Assess the morphology of the red blood cells.
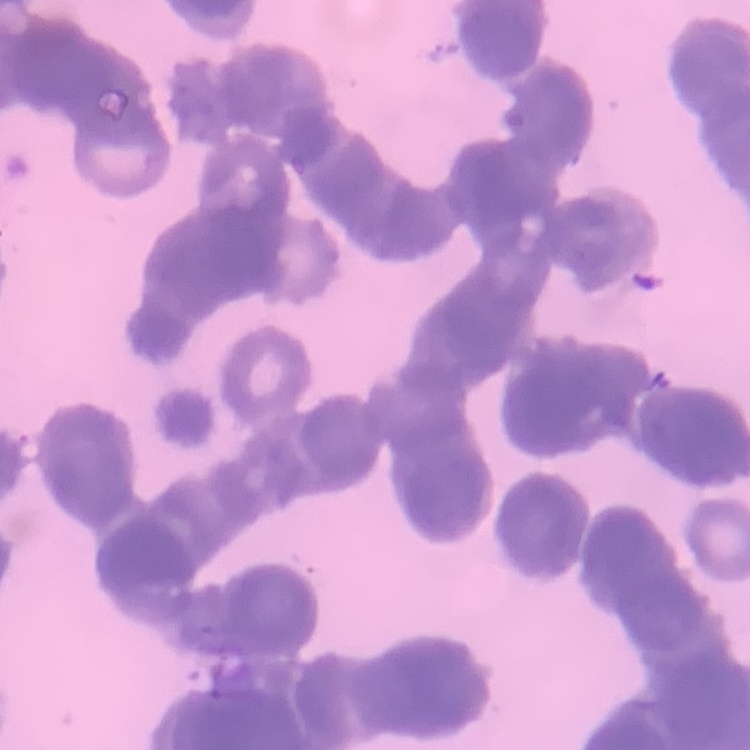
They show rouleaux formation.

Square crop of a larger photomicrograph. Stained with either Field's or Giemsa. Thin blood film.